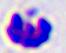

magnification: 400x
identification: leukocyte
modality: photomicrograph